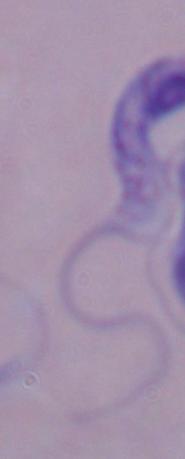
Summary:
  - Modality: photomicrograph
  - Magnification: 1000x
  - Identification: trypanosome